Classify this cell by malaria status.
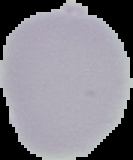
It is uninfected.

Summary:
  - Image size: 133×160 pixels
  - Image type: segmented cell region on a black background
  - Preparation: thin blood film